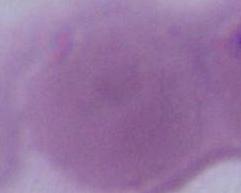

Captured at 1000x magnification. An erythrocyte is seen. Micrograph.